Describe the morphology of the red blood cells.
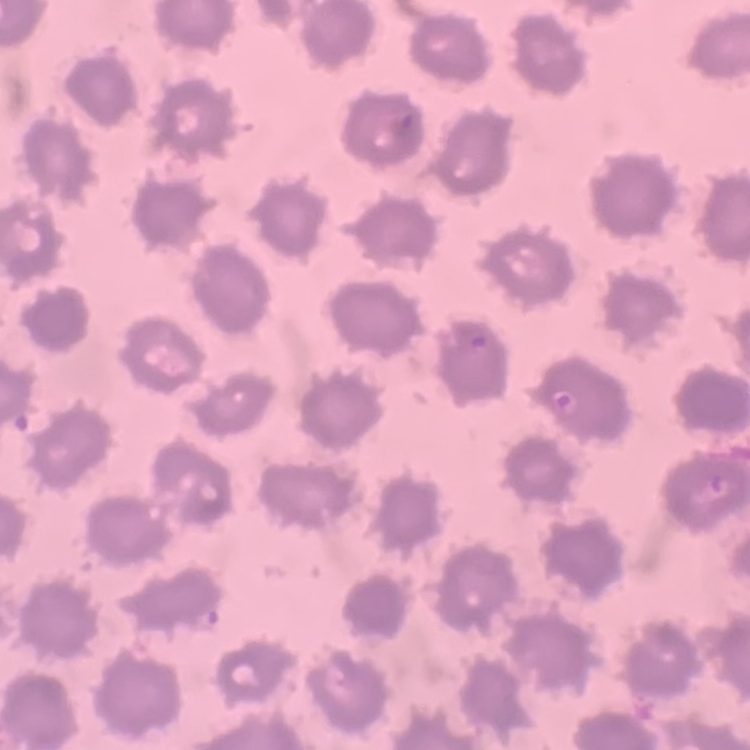
They show no rouleaux formation.

{
  "image_type": "square crop of a larger photomicrograph",
  "stain": "Field's or Giemsa",
  "preparation": "thin blood film"
}